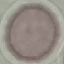

result = negative for malaria parasites
image type = cell patch, automatically extracted from a larger field of view and resized to 64 × 64 pixels
capture = smartphone through the microscope eyepiece
stain = Giemsa
preparation = thin blood smear